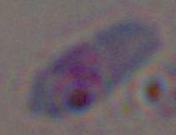
modality: micrograph
magnification: 1000x
identification: Toxoplasma gondii